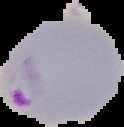 From a thin blood smear. Cell region segmented out of the field of view; the surrounding area is masked to black. Image is 124×127 pixels. Result: malaria parasites detected.